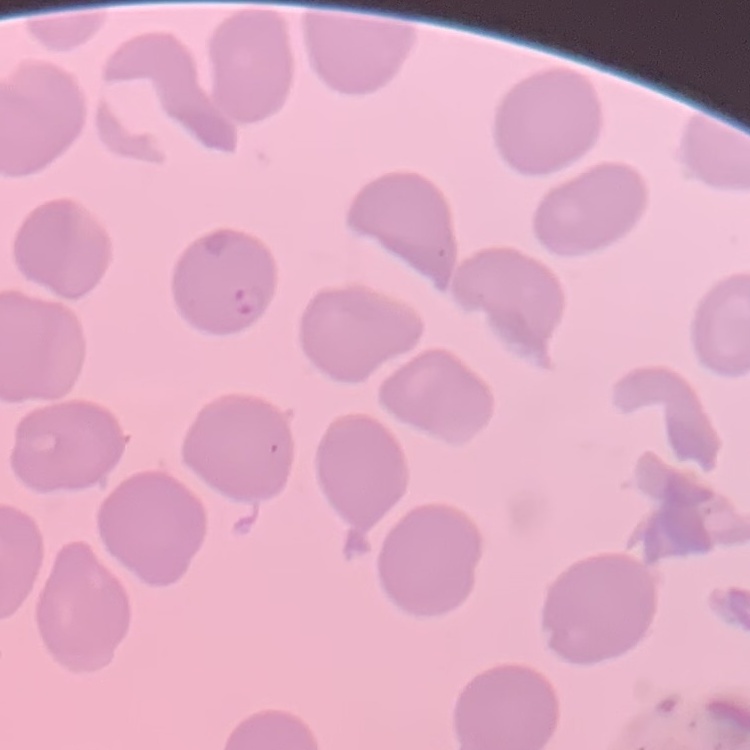

Summary:
  - Red blood cell morphology: no rouleaux formation
  - Stain: Field's or Giemsa
  - Image type: square crop of a larger photomicrograph
  - Preparation: thin blood film